Point out leukocytes.
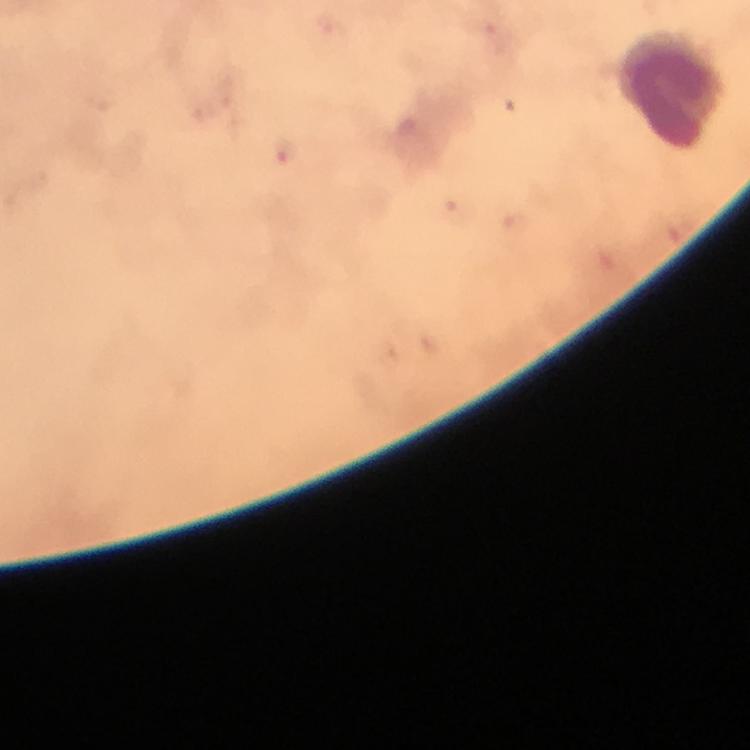

Approximate centers as {x, y} in pixels.
Leukocytes: {670, 88}.

Malaria parasite locations: {283, 150}. Photographed with a smartphone mounted on the microscope. 100x magnification. From a diagnostic examination for malaria. Thick blood film. Immersion oil was used. A crop from one field of view. Image is 750×750 pixels. Giemsa-stained preparation.